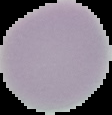

image type = segmented cell region on a black background
malaria status = uninfected
preparation = thin blood smear
image size = 112×115 pixels